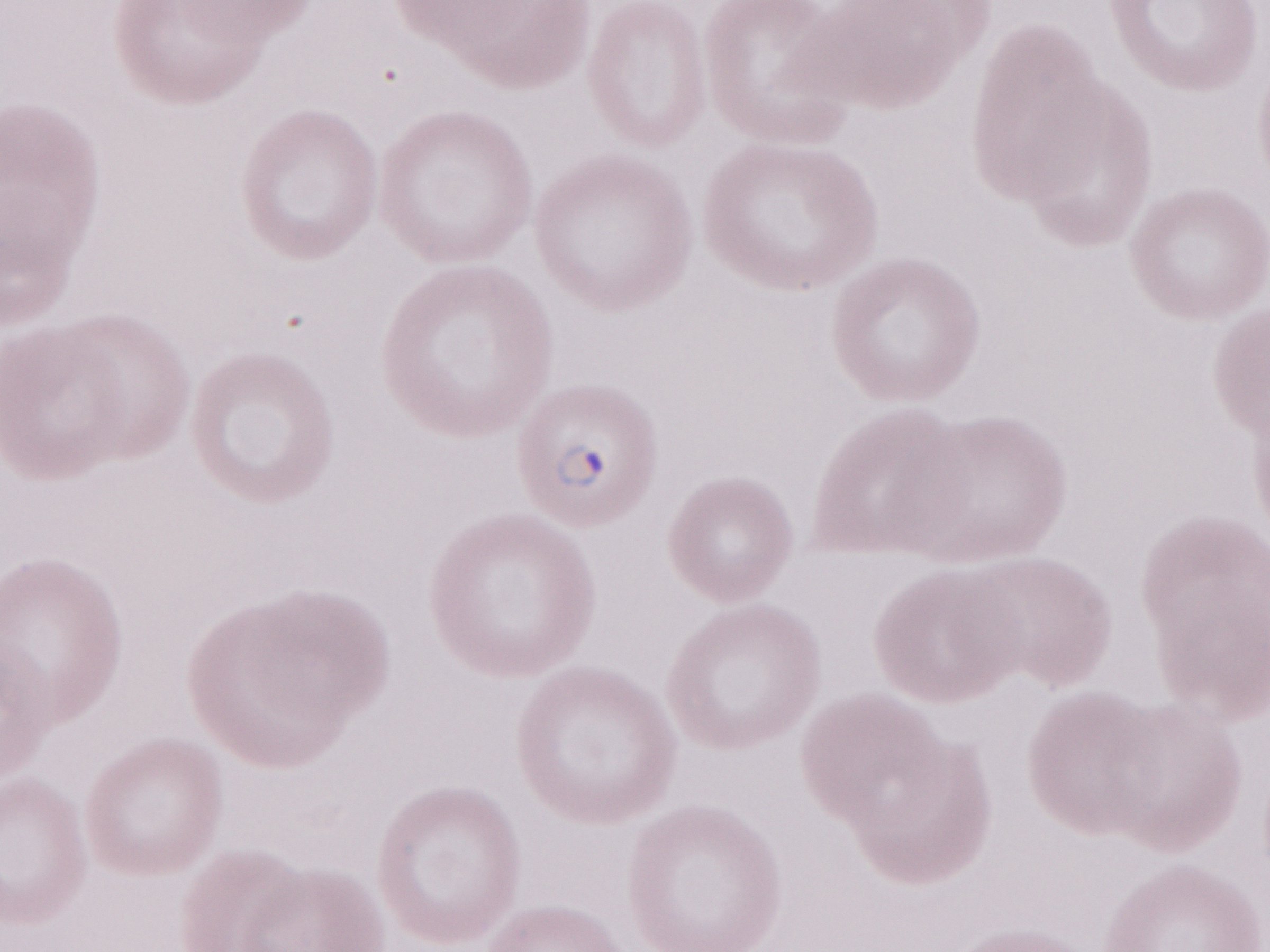

Olympus BX43 microscope and DP73 digital camera. Thin blood film. One field of this slide. May-Grünwald-Giemsa (MGG) stain. Patient diagnosis: malaria infection. Magnification: 1,000x. Image is 1270×952 pixels.